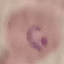
Summary:
  - Result: malaria parasites detected
  - Preparation: thin blood film
  - Image type: automatically extracted cell patch, resized to 64 × 64 pixels
  - Stain: Giemsa
  - Capture: smartphone camera at the microscope eyepiece